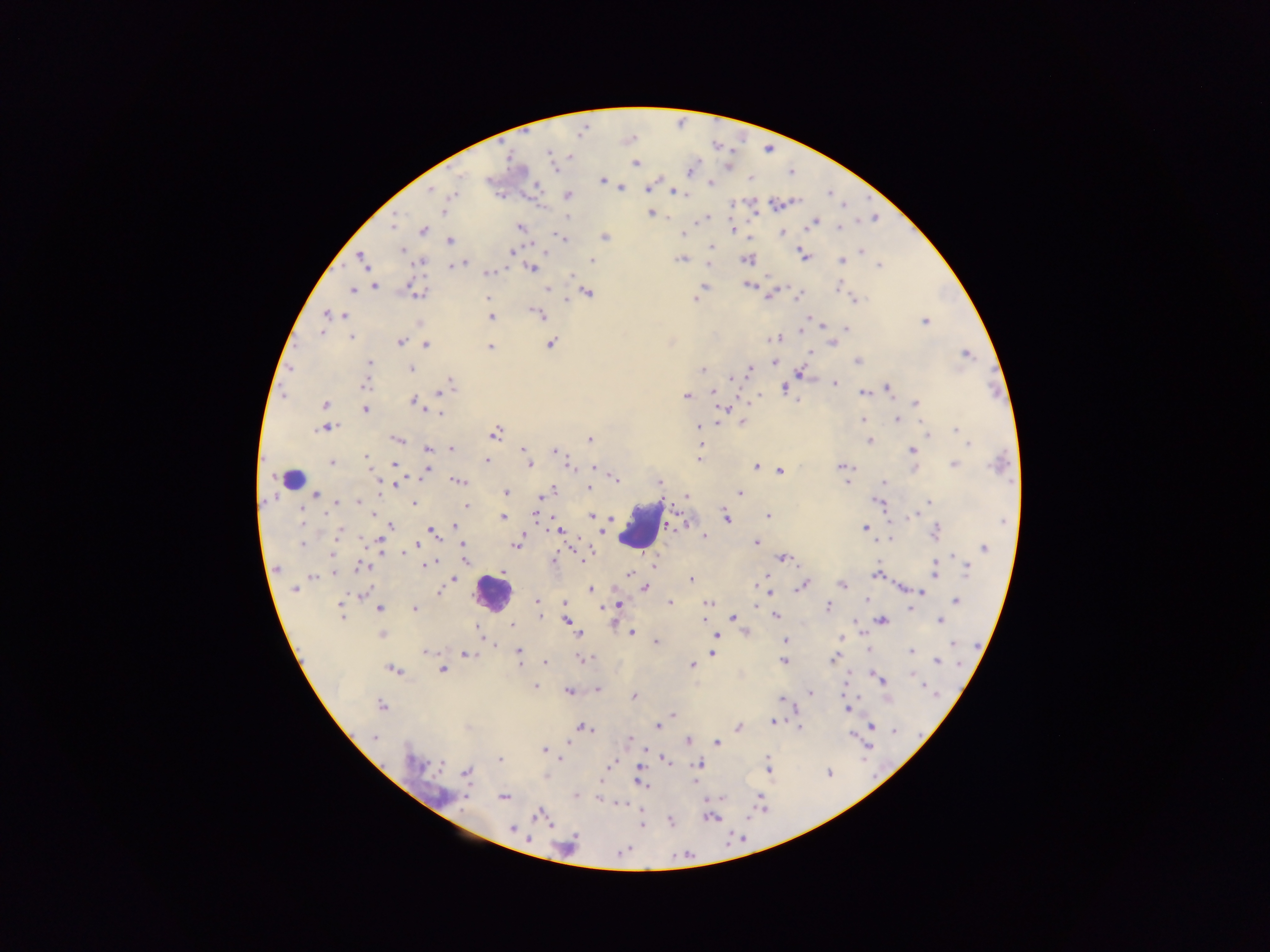
Approximate centers as (x, y) in pixels.
Summary:
  - Plasmodium parasite locations: (550, 155), (569, 156), (635, 163), (690, 170), (488, 179), (602, 180), (711, 183), (649, 187), (429, 188), (621, 188), (672, 191), (454, 193), (568, 196), (776, 204), (443, 211), (650, 213), (567, 218), (706, 219), (813, 222), (392, 224), (839, 226), (520, 227), (423, 230), (732, 230), (782, 232), (683, 234), (604, 237), (564, 239), (449, 240), (711, 246), (401, 250), (511, 251), (862, 251), (802, 254), (681, 259), (746, 259), (363, 260), (591, 260), (841, 261), (420, 262), (462, 262), (454, 264), (709, 264), (878, 265), (532, 268), (488, 273), (749, 285), (838, 286), (374, 287), (704, 287), (546, 288), (351, 289), (699, 291), (586, 292), (418, 293), (768, 294), (798, 295), (694, 297), (488, 298), (567, 299), (853, 300), (329, 315), (344, 315), (540, 315), (490, 317), (925, 320), (824, 325), (801, 328), (845, 329), (321, 331), (352, 337), (777, 337), (400, 342), (550, 343), (832, 343), (425, 344), (489, 347), (809, 352), (965, 354), (857, 360), (773, 361), (368, 362), (410, 369), (701, 369), (749, 370), (798, 373), (731, 378), (450, 380), (364, 383), (835, 383), (784, 387), (887, 387), (712, 392), (863, 392), (441, 393), (687, 395), (749, 400), (415, 401), (797, 401), (916, 403), (324, 404), (422, 406), (723, 408), (365, 409), (441, 413), (862, 419), (896, 419), (719, 423), (742, 423), (698, 426), (325, 427), (957, 430), (699, 431), (496, 432), (927, 432), (397, 439), (589, 440), (868, 440), (968, 442), (427, 448), (451, 448), (523, 448), (911, 450), (555, 451), (365, 456), (526, 459), (698, 459), (487, 461), (331, 462), (394, 464), (954, 464), (529, 465), (567, 465), (841, 465), (756, 466), (593, 468), (914, 468), (426, 471), (780, 471), (612, 477), (375, 479), (659, 481), (884, 481), (458, 482), (847, 482), (395, 485), (588, 488), (505, 492), (739, 492), (548, 493), (310, 495), (685, 496), (541, 498), (336, 502), (358, 502), (928, 502), (878, 503), (414, 504), (465, 505), (374, 513), (536, 514), (591, 516), (767, 516), (912, 516), (502, 518), (724, 518), (608, 519), (678, 524), (392, 525), (456, 526), (866, 528), (431, 529), (558, 529), (339, 530), (935, 531), (598, 536), (702, 536), (889, 538), (379, 541), (416, 543), (463, 543), (516, 543), (756, 543), (303, 544), (983, 548), (400, 550), (332, 554), (783, 557), (583, 559), (464, 560), (552, 561), (423, 564), (654, 565), (363, 566), (965, 567), (276, 568), (934, 570), (503, 571), (333, 573), (630, 574), (878, 574), (313, 576), (453, 579), (691, 580), (757, 583), (802, 585), (842, 585), (644, 588), (901, 588), (591, 589), (765, 589), (295, 590), (649, 590), (920, 591), (438, 592), (769, 592), (363, 593), (536, 599), (866, 600), (955, 600), (565, 602), (670, 602), (708, 603), (618, 605), (756, 605), (827, 606), (909, 606), (379, 608), (414, 609), (341, 610), (774, 615), (539, 616), (733, 617), (881, 620), (939, 620), (566, 621), (704, 621), (511, 625), (478, 627), (746, 631), (631, 632), (382, 634), (579, 635), (716, 635), (840, 637), (785, 640), (656, 642), (494, 645), (427, 651), (910, 651), (519, 652), (712, 653), (466, 654), (834, 658), (581, 659), (782, 660), (936, 661), (543, 662), (691, 665), (393, 669), (442, 670), (912, 674), (881, 679), (535, 686), (925, 686), (597, 689), (844, 689), (569, 692), (809, 693), (634, 697), (783, 699), (381, 706), (846, 709), (672, 714), (773, 721), (870, 724), (656, 726), (583, 727), (798, 727), (738, 728), (852, 735), (375, 738), (629, 740), (687, 741), (567, 742), (717, 742), (543, 749), (560, 758), (665, 759), (499, 760), (611, 763), (698, 763), (768, 767), (639, 770), (466, 772), (639, 781), (599, 782), (695, 782), (576, 796), (758, 796), (504, 797), (599, 798), (619, 803), (538, 815), (712, 818), (671, 821), (641, 825), (512, 829)
  - Leukocyte locations: (288, 478), (639, 526), (492, 593)
  - Image size: 1270×952 pixels
  - Field of view: single
  - Country: Ghana
  - Preparation: thick blood smear
  - Capture: mobile-phone photograph through a microscope